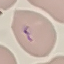

result = malaria parasites detected
capture = smartphone through the microscope eyepiece
image type = automatically extracted cell patch, resized to 64 × 64 pixels
stain = Giemsa
preparation = thin smear